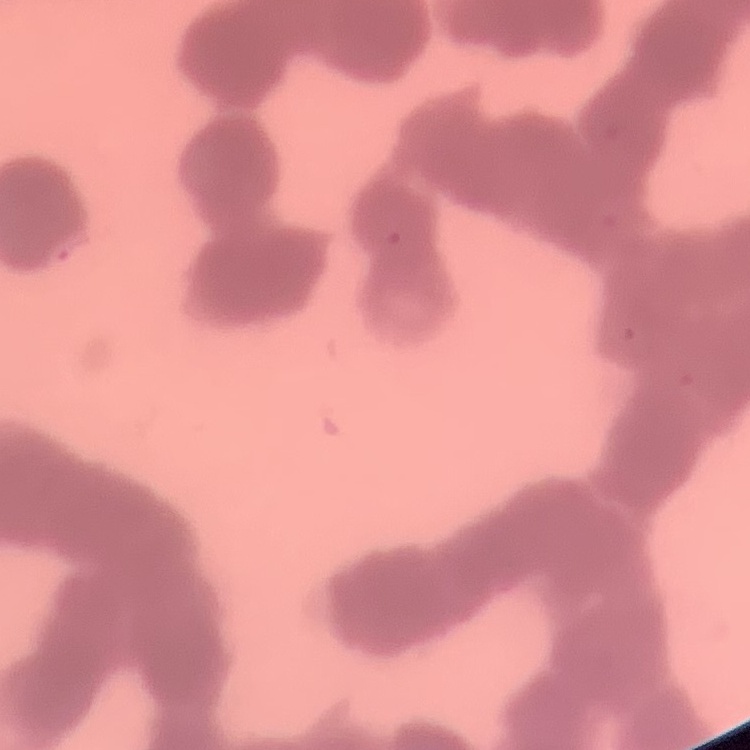

Summary:
  - Red blood cell morphology: rouleaux formation
  - Preparation: thin blood smear
  - Stain: Field's or Giemsa
  - Image type: one tile cut from a larger photomicrograph